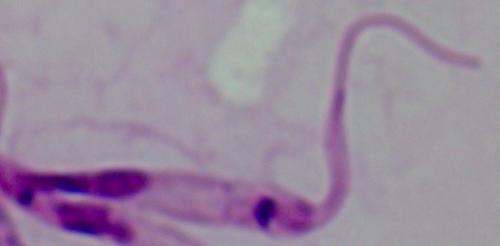
modality = micrograph
identification = Leishmania
magnification = 1000x